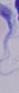

Summary:
  - Modality: micrograph
  - Magnification: 1000x
  - Identification: trypanosome